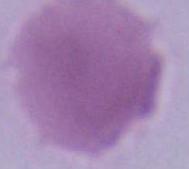

Photomicrograph. A red blood cell is shown. Captured at 1000x magnification.